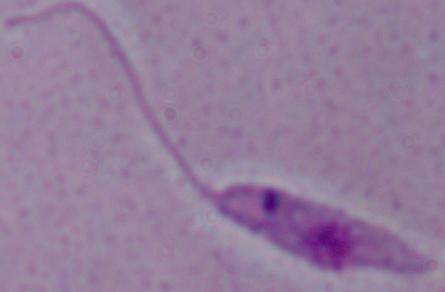

Summary:
  - Modality: micrograph
  - Magnification: 1000x
  - Identification: Leishmania